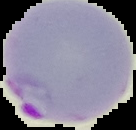
Image is 136×130 pixels. Segmented cell region on a black background. From a thin blood smear. Result: Plasmodium parasites detected.